Locate every Plasmodium vivax-infected red blood cell.
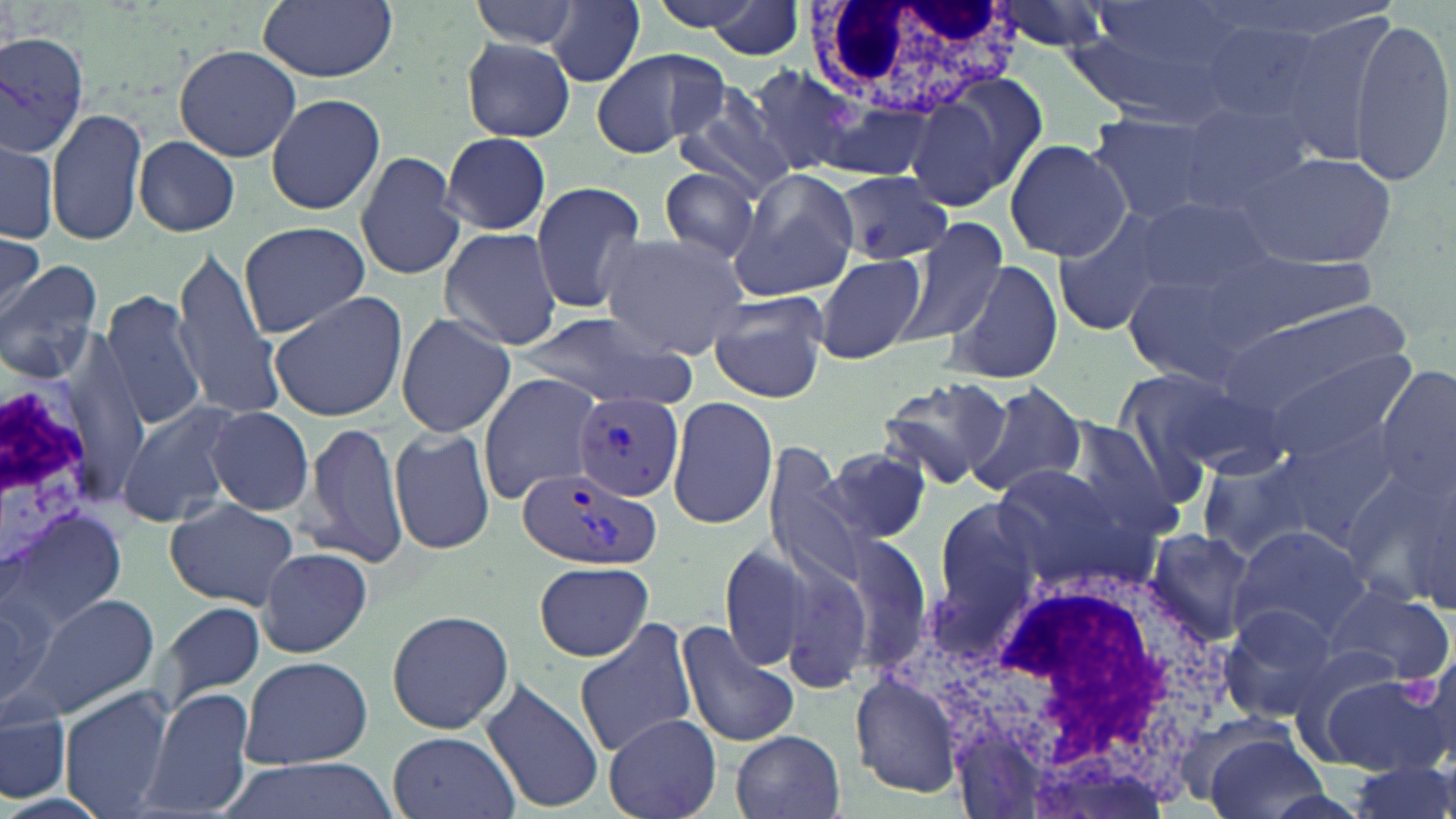
Approximate bounding boxes as [x1, y1, x2, y2] in pixels.
Plasmodium vivax-infected red blood cells: [574, 390, 685, 502], [516, 467, 660, 573].

Summary:
  - Platelet locations: [1403, 675, 1439, 711]
  - White blood cell locations: [812, 2, 1015, 126], [1, 369, 116, 581], [893, 567, 1235, 805]
  - Uninfected red blood cell locations: [258, 0, 398, 81], [468, 0, 586, 53], [643, 0, 782, 34], [987, 0, 1117, 54], [687, 1, 809, 59], [546, 3, 650, 87], [1060, 11, 1245, 123], [1350, 14, 1454, 185], [0, 31, 89, 157], [460, 36, 577, 143], [174, 44, 301, 163], [590, 46, 729, 158], [748, 68, 875, 179], [906, 78, 1035, 211], [264, 92, 388, 216], [676, 93, 801, 200], [46, 106, 147, 247], [1179, 107, 1314, 212], [1085, 111, 1228, 225], [441, 132, 551, 235], [133, 135, 240, 236], [1003, 138, 1133, 262], [1, 139, 58, 243], [1236, 148, 1396, 269], [355, 149, 466, 283], [659, 165, 762, 266], [726, 170, 858, 302], [838, 173, 951, 267], [528, 182, 651, 315], [1124, 192, 1280, 307], [1049, 208, 1178, 336], [891, 218, 1013, 346], [237, 222, 370, 337], [439, 227, 563, 351], [596, 230, 751, 357], [0, 237, 44, 320], [0, 243, 71, 350], [167, 243, 287, 422], [1223, 250, 1379, 332], [813, 253, 928, 365], [944, 258, 1063, 386], [0, 261, 104, 386], [100, 287, 209, 432], [706, 290, 834, 403], [268, 292, 409, 423], [1217, 298, 1411, 420], [517, 312, 699, 406], [397, 313, 516, 436], [1257, 352, 1415, 472], [1112, 364, 1265, 495], [1376, 364, 1454, 494], [475, 372, 602, 503], [875, 373, 1015, 491], [968, 384, 1088, 498], [668, 394, 776, 531], [115, 398, 248, 530], [205, 407, 315, 517], [1272, 413, 1407, 544], [302, 418, 409, 568], [1053, 418, 1187, 540], [389, 427, 498, 556], [761, 443, 870, 590], [823, 446, 933, 548], [1193, 448, 1331, 561], [991, 464, 1152, 587], [1348, 464, 1456, 609], [933, 499, 1045, 616], [164, 500, 300, 609], [7, 502, 126, 641], [1229, 522, 1370, 643], [1143, 528, 1259, 643], [833, 530, 935, 672], [765, 541, 885, 693], [720, 544, 810, 670], [258, 547, 373, 657], [533, 560, 654, 661], [1321, 584, 1452, 684], [0, 589, 96, 718], [24, 591, 157, 716], [151, 599, 266, 715], [1216, 603, 1339, 721], [385, 608, 514, 734], [573, 619, 698, 761], [674, 620, 801, 748], [1290, 639, 1414, 741], [238, 653, 372, 769], [1321, 670, 1450, 776], [851, 676, 963, 798], [480, 677, 604, 814], [137, 687, 256, 819], [59, 689, 174, 819], [0, 705, 71, 804], [603, 714, 722, 819], [1194, 723, 1327, 819], [388, 730, 518, 819], [732, 730, 846, 819], [217, 756, 398, 819], [1341, 761, 1456, 819]
  - Slide-level diagnosis: Plasmodium vivax
  - Field of view: one of a larger specimen
  - Image size: 1456×819 pixels
  - Preparation: thin blood smear
  - Stain: May-Grünwald-Giemsa
  - Modality: light microscopy
  - Magnification: 1000x